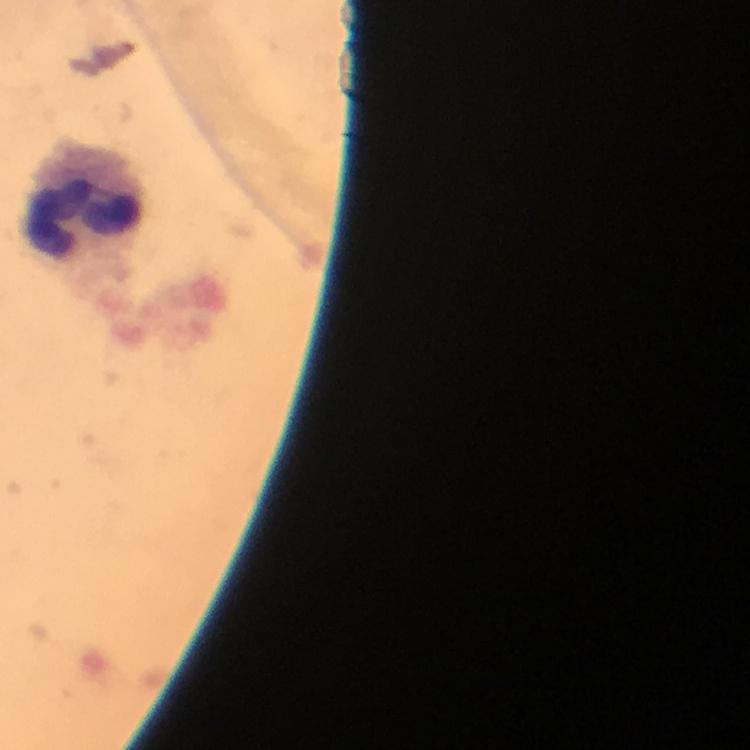

Approximate centers as [x, y] in pixels. Leukocyte locations: [81, 206]. From a malaria diagnostic workup. Plasmodium parasites: none seen. Image is 750×750 pixels. 100x magnification. Smartphone photograph taken through a microscope. Thick smear. Cropped region of a single field of view. Immersion oil was used. Giemsa stain.